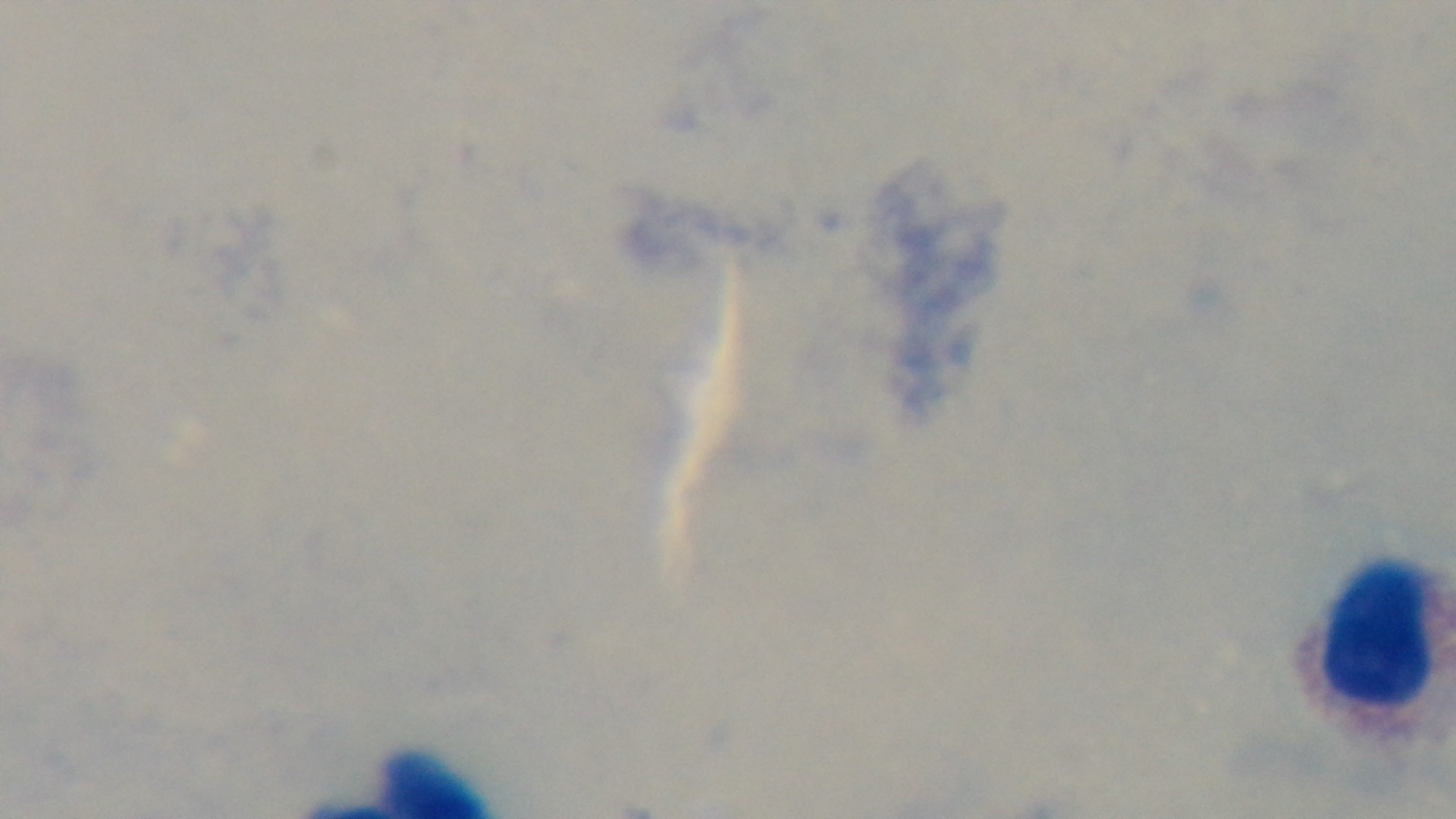
Summary:
  - Capture: mounted 4K digital camera
  - Field of view: one from the slide
  - Stain: Giemsa
  - Modality: light microscopy
  - Malaria status: uninfected
  - Objective: 100x oil immersion
  - Preparation: thick